Classify this cell by malaria status.
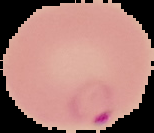

Parasitized.

Cell region segmented out of the field of view; the surrounding area is masked to black. From a thin blood smear. Image is 154×133 pixels.